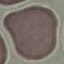

Summary:
  - Malaria status: uninfected
  - Image type: cell patch, automatically extracted from a larger field of view and resized to 64 × 64 pixels
  - Stain: Giemsa
  - Preparation: thin blood film
  - Capture: smartphone through the microscope eyepiece